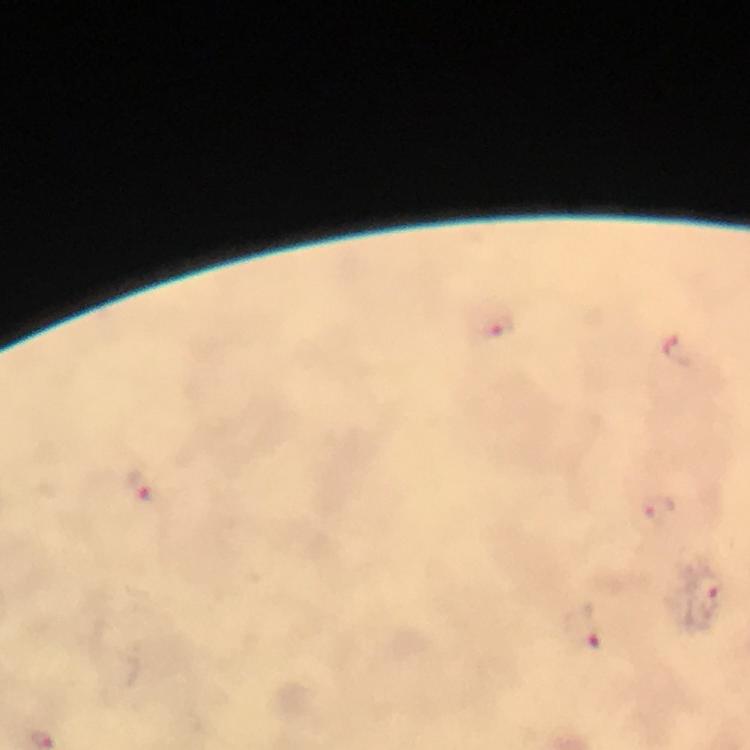
stain = Giemsa
cropped from = one field of view
immersion oil = applied
capture = smartphone camera through the microscope
malaria parasite locations = approximate centers as {x, y} in pixels: {498, 329}, {138, 486}, {659, 507}, {705, 587}, {584, 628}
image size = 750×750 pixels
preparation = thick blood smear
context = from a diagnostic examination for malaria
magnification = 100x